State which cell type is depicted.
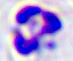

A leukocyte.

{
  "magnification": "400x",
  "modality": "micrograph"
}